Outline each blood parasite and name the species.
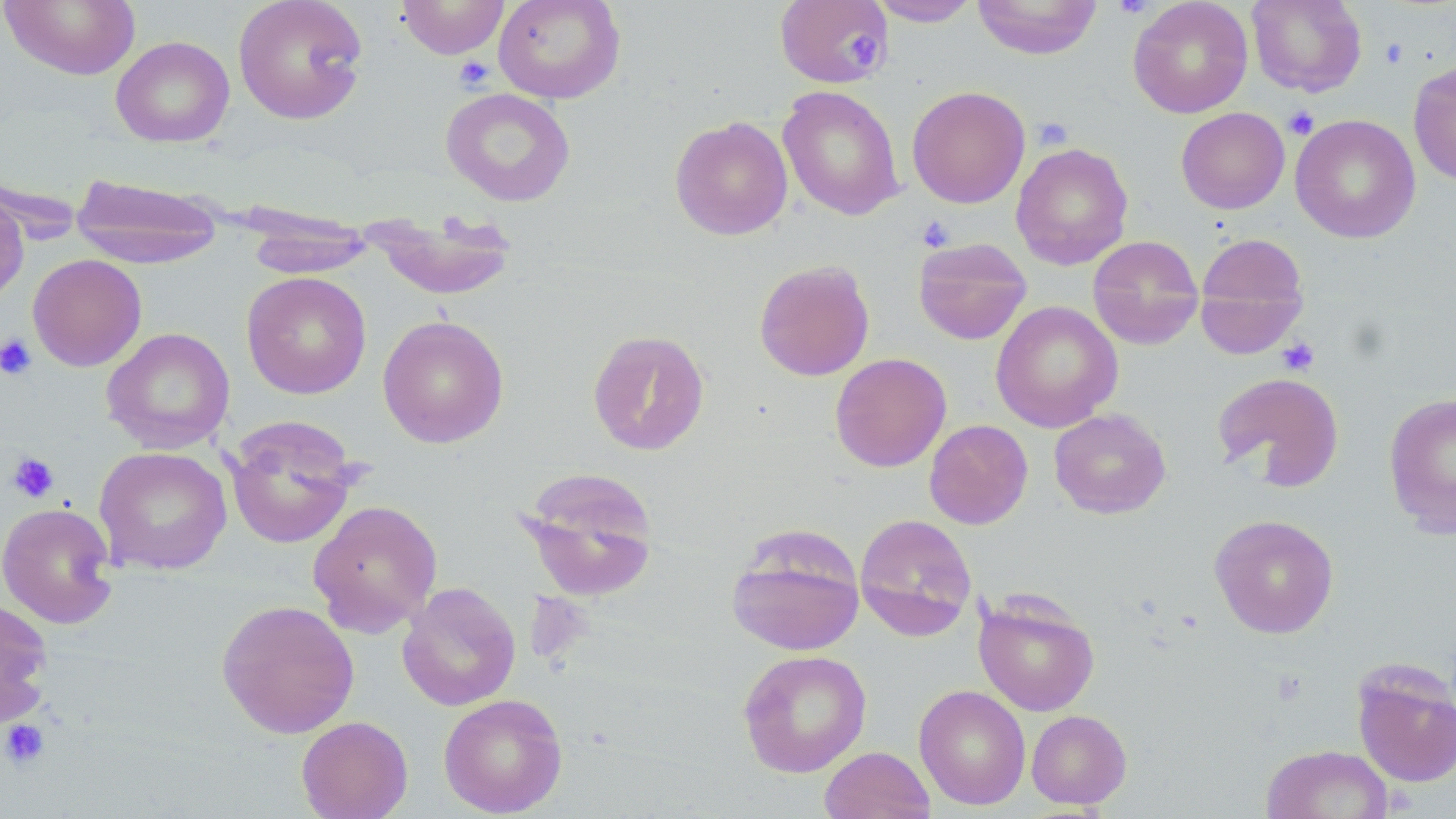
No blood parasites observed.

Approximate bounding boxes as (x1, y1, x2, y2) in pixels. Platelet locations: (1111, 0, 1156, 19), (845, 34, 881, 70), (1379, 39, 1409, 68), (453, 55, 495, 92), (1283, 106, 1320, 140), (1031, 117, 1073, 151), (916, 216, 956, 251), (0, 333, 37, 380), (1276, 337, 1320, 375), (7, 452, 60, 504), (1, 719, 50, 770). Uninfected red blood cell locations: (0, 0, 141, 80), (233, 0, 369, 125), (395, 0, 508, 59), (492, 0, 626, 104), (775, 0, 892, 88), (868, 0, 982, 27), (972, 0, 1102, 59), (1128, 0, 1254, 118), (1247, 0, 1367, 97), (110, 36, 235, 147), (1408, 61, 1456, 185), (778, 86, 904, 221), (907, 86, 1030, 208), (440, 87, 576, 207), (1176, 107, 1290, 214), (1290, 114, 1420, 243), (670, 116, 793, 240), (1011, 142, 1133, 270), (70, 173, 226, 268), (0, 186, 29, 307), (244, 208, 374, 278), (368, 209, 518, 302), (1195, 233, 1309, 346), (1087, 236, 1205, 349), (913, 237, 1032, 346), (27, 253, 147, 371), (753, 260, 875, 381), (241, 271, 372, 399), (991, 300, 1123, 433), (377, 315, 509, 449), (101, 327, 235, 454), (587, 329, 711, 455), (830, 353, 951, 472), (1212, 372, 1345, 490), (1383, 393, 1456, 539), (1049, 409, 1172, 519), (224, 418, 360, 550), (924, 420, 1033, 529), (94, 446, 232, 576), (517, 466, 659, 601), (307, 499, 444, 636), (1, 502, 119, 629), (854, 513, 977, 641), (1209, 514, 1339, 638), (726, 527, 865, 656), (397, 582, 521, 712), (973, 591, 1101, 717), (0, 598, 54, 731), (215, 599, 360, 738), (737, 649, 872, 777), (1352, 664, 1456, 788), (914, 684, 1031, 810), (438, 693, 567, 817), (1026, 709, 1131, 810), (296, 715, 413, 819), (1261, 744, 1394, 819), (819, 746, 935, 819). Slide-level diagnosis: no evidence of blood parasites. Single field of view. Thin blood film. May-Grünwald-Giemsa-stained preparation. Light microscopy. 1000x magnification. Image is 1456×819 pixels.